Identify the blood parasite species.
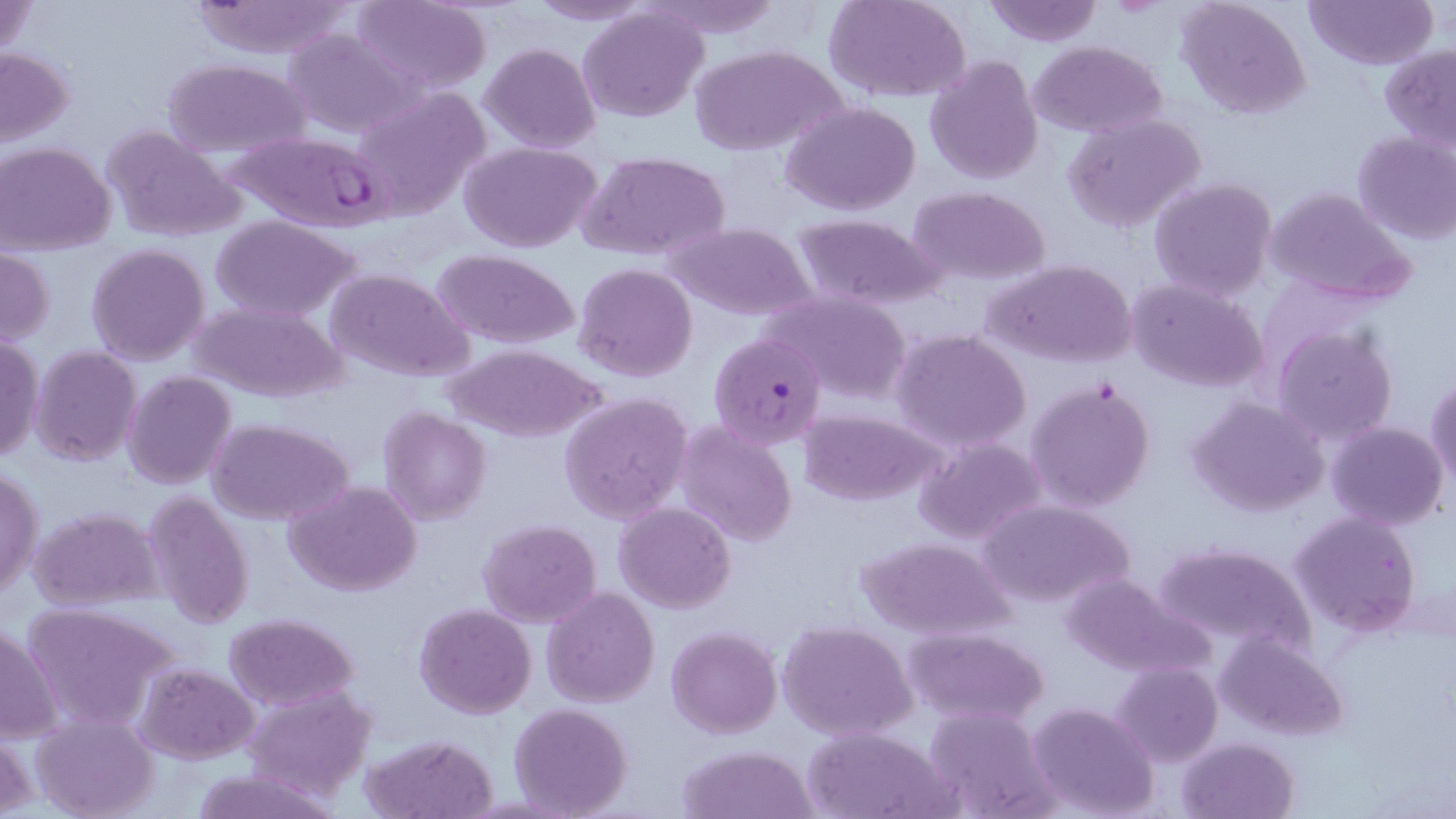
Plasmodium falciparum.

preparation: thin blood film
modality: optical microscopy
field_of_view: one of a larger specimen
image_size: 1456×819 pixels
uninfected_red_blood_cell_locations: 'approximate bounding boxes as (x1,y1)-(x2,y2) corner pairs in pixels: (185,0)-(365,60), (352,0)-(491,93), (521,0)-(661,25), (640,0)-(785,37), (827,0)-(970,102), (984,0)-(1102,47), (1178,0)-(1312,118), (1305,0)-(1437,71), (1,1)-(40,59), (577,6)-(709,125), (282,28)-(417,137), (1029,40)-(1169,137), (479,41)-(601,153), (691,44)-(846,156), (0,46)-(75,147), (1380,46)-(1456,151), (924,54)-(1043,185), (164,59)-(313,158), (348,85)-(489,215), (781,101)-(922,217), (1064,113)-(1207,236), (102,127)-(246,241), (1352,131)-(1456,246), (461,140)-(602,252), (1,142)-(116,255), (577,150)-(732,261), (1149,176)-(1278,301), (906,186)-(1051,286), (1265,188)-(1416,307), (789,213)-(944,308), (209,215)-(360,321), (670,223)-(817,320), (87,243)-(210,366), (0,248)-(53,348), (429,248)-(580,348), (984,258)-(1139,368), (574,262)-(696,383), (324,268)-(474,383), (1124,276)-(1271,394), (761,288)-(914,403), (190,299)-(348,402), (1272,324)-(1398,445), (891,327)-(1032,454), (0,335)-(44,465), (446,345)-(604,441), (29,346)-(141,466), (122,371)-(236,489), (1427,375)-(1456,493), (1026,378)-(1156,513), (559,391)-(693,523), (1188,395)-(1330,517), (378,408)-(492,525), (798,408)-(945,505), (208,418)-(352,525), (674,419)-(800,550), (1326,421)-(1448,532), (914,436)-(1046,546), (1,465)-(42,600), (285,481)-(423,596), (142,491)-(254,630), (974,497)-(1134,608), (614,502)-(737,612), (29,506)-(165,611), (1288,509)-(1422,635), (478,518)-(601,626), (856,534)-(1015,640), (1152,539)-(1318,656), (1058,573)-(1208,677), (542,587)-(660,708), (21,601)-(178,733), (413,604)-(538,719), (224,613)-(360,710), (778,619)-(917,740), (1,620)-(61,745), (665,626)-(782,738), (903,626)-(1049,727), (1215,632)-(1349,740), (1112,661)-(1222,767), (134,662)-(258,764), (242,684)-(376,802), (1026,701)-(1160,819), (508,702)-(633,818), (923,706)-(1057,818), (30,713)-(158,819), (2,726)-(39,817), (801,726)-(953,818), (361,733)-(498,818), (1178,737)-(1300,819), (677,745)-(819,819), (185,768)-(339,819)'
magnification: 1000x
plasmodium_falciparum_infected_red_blood_cell_locations: 'approximate bounding boxes as (x1,y1)-(x2,y2) corner pairs in pixels: (226,130)-(392,230), (708,322)-(839,445)'
stain: May-Grünwald-Giemsa